Outline each blood parasite and name the species.
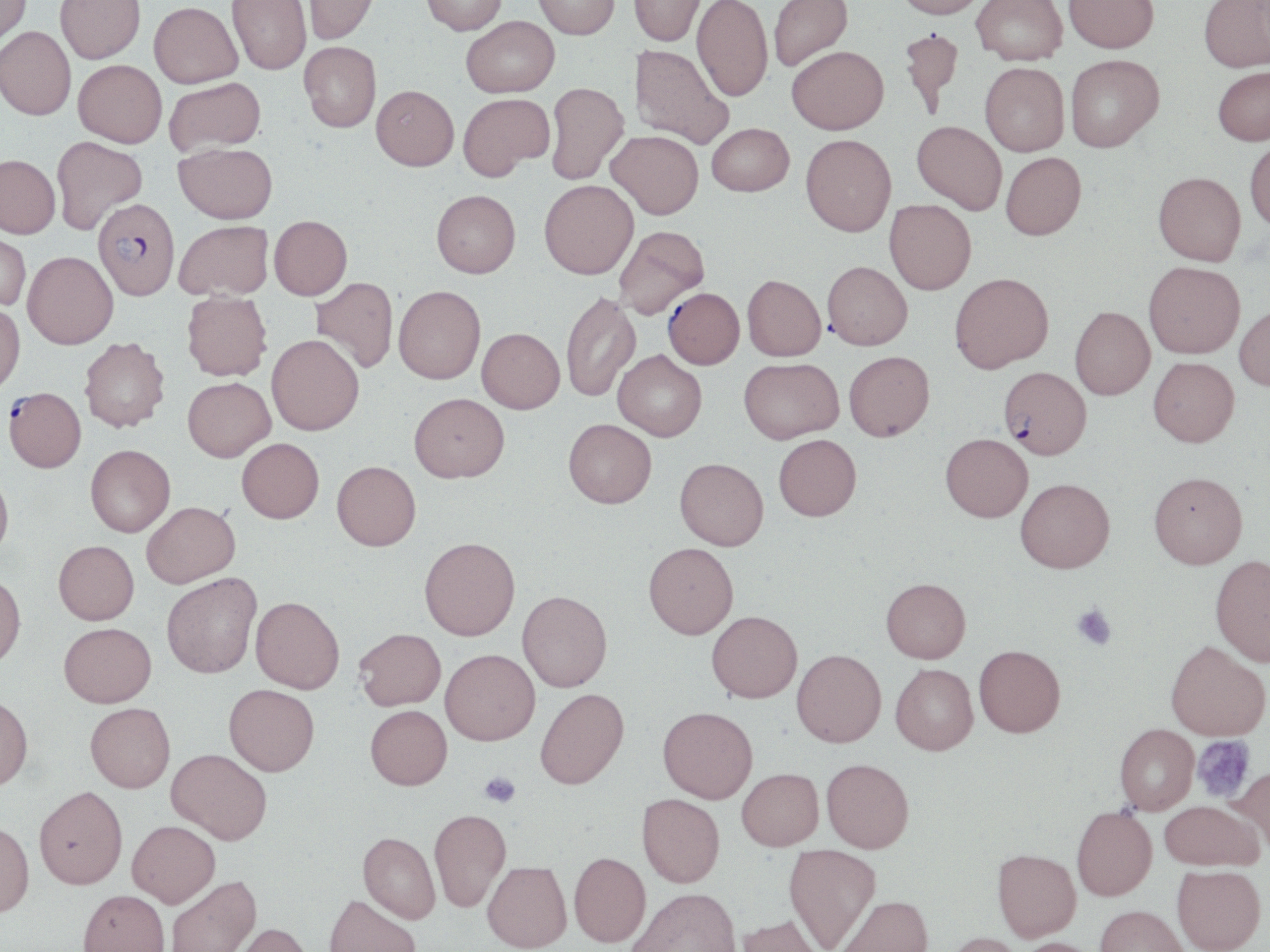
Approximate bounding boxes as (x1,y1)-(x2,y2) corner pairs in pixels.
Plasmodium falciparum-infected red blood cells: (93,198)-(180,299), (663,287)-(744,369), (998,366)-(1092,459), (4,387)-(85,472).
No Plasmodium ovale, Plasmodium malariae, Plasmodium vivax, Babesia divergens, or Trypanosoma brucei observed.

Summary:
  - Platelet locations: (1072,603)-(1117,650), (1192,735)-(1255,803), (479,771)-(521,807)
  - Uninfected red blood cell locations: (0,0)-(31,51), (56,0)-(145,63), (227,0)-(311,75), (303,0)-(379,45), (420,0)-(508,35), (533,0)-(619,39), (629,0)-(705,46), (692,0)-(773,102), (768,0)-(853,72), (894,0)-(988,18), (972,0)-(1068,66), (1064,0)-(1158,54), (1199,0)-(1270,72), (148,2)-(243,88), (462,16)-(559,97), (0,27)-(76,120), (898,27)-(965,118), (299,41)-(381,132), (630,45)-(734,149), (787,45)-(888,133), (1065,54)-(1164,152), (74,60)-(167,148), (980,62)-(1069,156), (1212,66)-(1270,146), (164,78)-(265,157), (545,82)-(628,185), (371,84)-(459,170), (458,93)-(554,180), (912,120)-(1006,214), (707,123)-(794,196), (607,130)-(703,219), (800,134)-(896,236), (51,135)-(148,235), (1245,138)-(1270,232), (174,142)-(278,223), (1001,152)-(1086,240), (0,155)-(61,238), (1153,171)-(1246,265), (539,180)-(638,279), (431,190)-(520,277), (884,199)-(976,295), (269,215)-(352,299), (174,220)-(273,301), (614,225)-(709,319), (0,231)-(31,312), (23,251)-(118,348), (822,261)-(912,350), (1144,261)-(1245,359), (950,272)-(1054,372), (742,275)-(826,361), (311,277)-(398,373), (393,285)-(485,383), (182,291)-(272,381), (560,292)-(640,402), (0,302)-(25,395), (1234,304)-(1270,391), (1070,306)-(1155,399), (477,328)-(565,413), (267,334)-(364,435), (79,338)-(170,432), (613,350)-(707,440), (844,350)-(934,440), (739,357)-(843,443), (1148,357)-(1239,446), (183,377)-(275,461), (409,392)-(509,482), (563,419)-(656,508), (940,433)-(1033,522), (774,434)-(861,521), (237,438)-(324,522), (86,445)-(175,537), (675,458)-(768,550), (332,461)-(420,550), (0,470)-(13,561), (1149,471)-(1248,568), (1015,478)-(1115,572), (141,501)-(240,587), (419,537)-(520,640), (53,540)-(139,624), (644,542)-(738,638), (1210,555)-(1270,666), (161,572)-(261,678), (0,573)-(26,669), (881,577)-(970,662), (517,590)-(612,691), (250,596)-(345,693), (707,610)-(802,702), (59,622)-(156,706), (354,628)-(446,710), (1166,640)-(1270,739), (974,644)-(1065,737), (440,648)-(539,745), (792,649)-(886,747), (890,663)-(978,754), (224,683)-(320,775), (534,688)-(629,789), (0,694)-(33,790), (85,702)-(175,792), (365,705)-(452,789), (658,706)-(758,803), (1114,723)-(1199,814), (166,748)-(272,844), (822,758)-(914,853), (1230,765)-(1270,853), (737,768)-(824,850), (34,785)-(128,888), (637,793)-(725,887), (1159,800)-(1261,869), (1071,805)-(1157,901), (429,808)-(511,912), (0,820)-(35,916), (127,820)-(220,907), (358,832)-(440,923), (784,845)-(881,950), (992,848)-(1081,941), (569,852)-(651,946), (483,861)-(571,951), (1171,865)-(1266,952), (166,874)-(261,952), (628,887)-(742,952), (78,889)-(170,952), (324,894)-(420,952), (835,895)-(933,952), (1095,904)-(1187,952), (734,913)-(828,952), (229,922)-(313,952), (945,932)-(1026,952), (1014,937)-(1104,952)
  - Slide-level diagnosis: Plasmodium falciparum
  - Image size: 1270×952 pixels
  - Modality: optical microscopy
  - Field of view: single
  - Preparation: thin blood smear
  - Stain: May-Grünwald-Giemsa
  - Magnification: 1000x